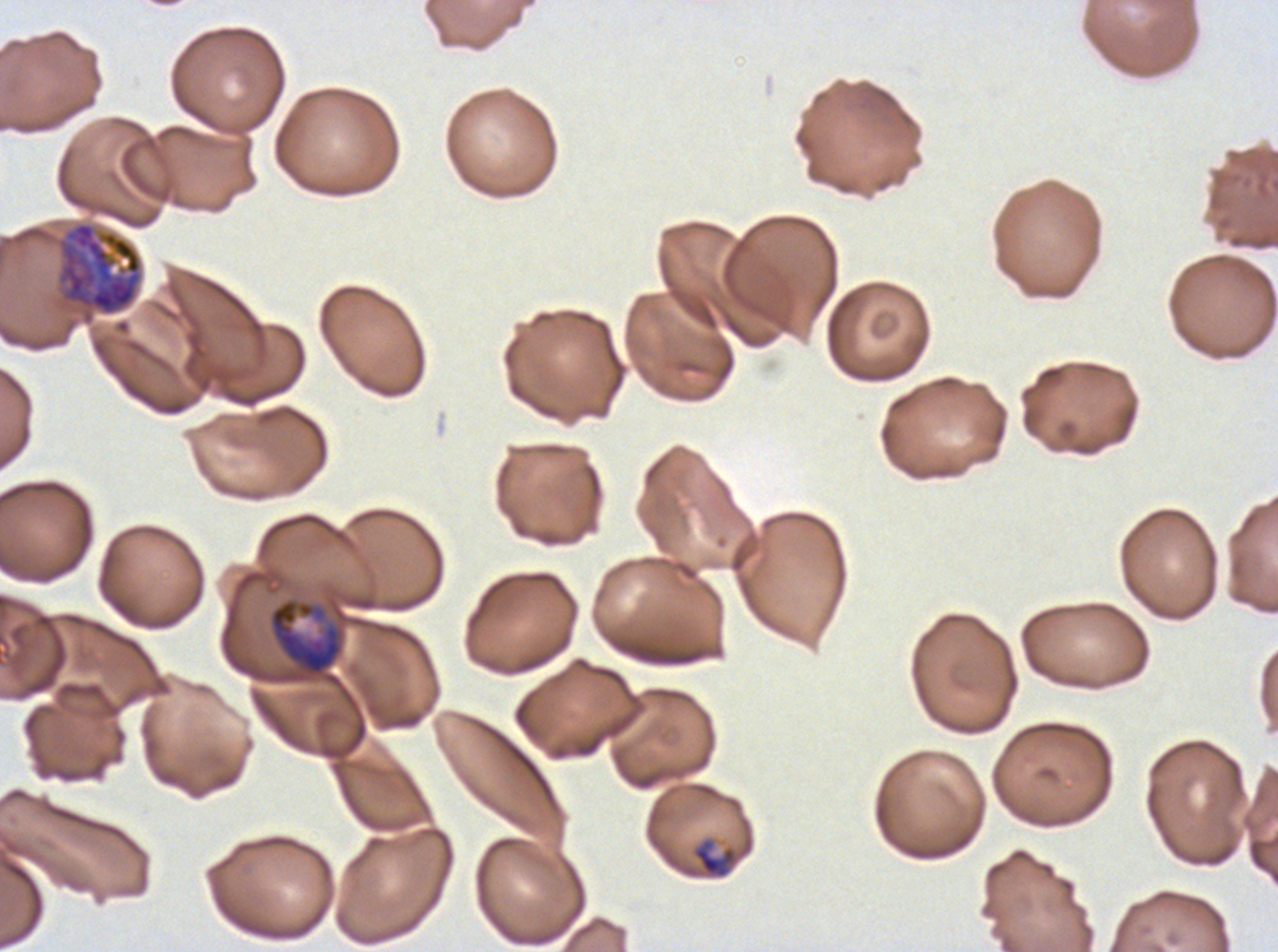

{
  "image_size": "1278×952 pixels",
  "late_ring_early_trophozoite_locations": "approximate bounding boxes as [x1, y1, x2, y2] in pixels: [692, 837, 738, 880]",
  "early_schizont_locations": "approximate bounding boxes as [x1, y1, x2, y2] in pixels: [57, 221, 142, 316]",
  "life_cycle_stages_observed": "late-ring/early-trophozoite, late trophozoite, early schizont",
  "preparation": "thin blood smear",
  "late_trophozoite_locations": "approximate bounding boxes as [x1, y1, x2, y2] in pixels: [268, 598, 344, 677]",
  "field_of_view": "one sub-image of a larger composite",
  "specimen": "P. falciparum cultured ex vivo for 24 to 48 hours, from a patient in The Gambia",
  "stain": "Giemsa"
}